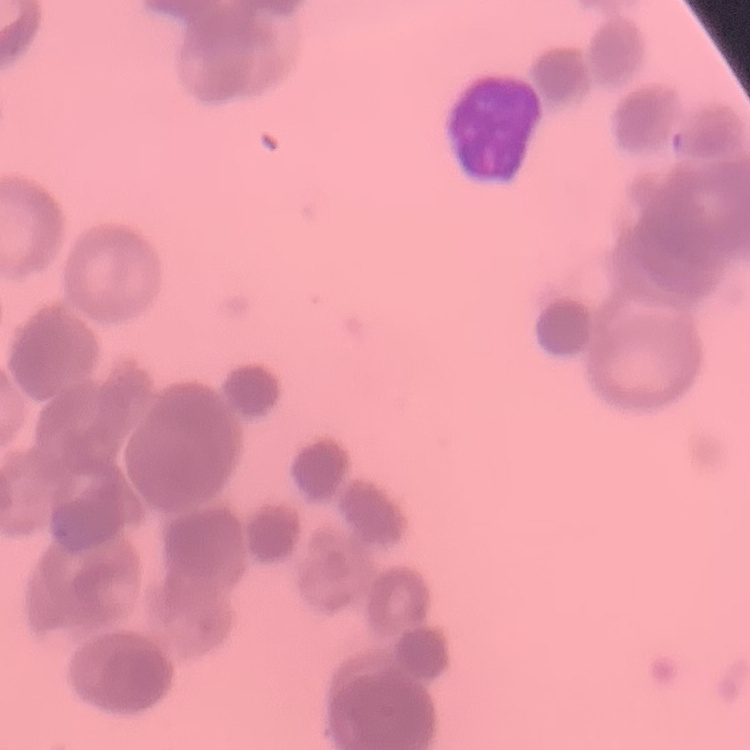 The erythrocytes exhibit rouleaux formation. One tile cut from a larger photomicrograph. Field's or Giemsa stain. Thin peripheral smear.